Classify the preparation.
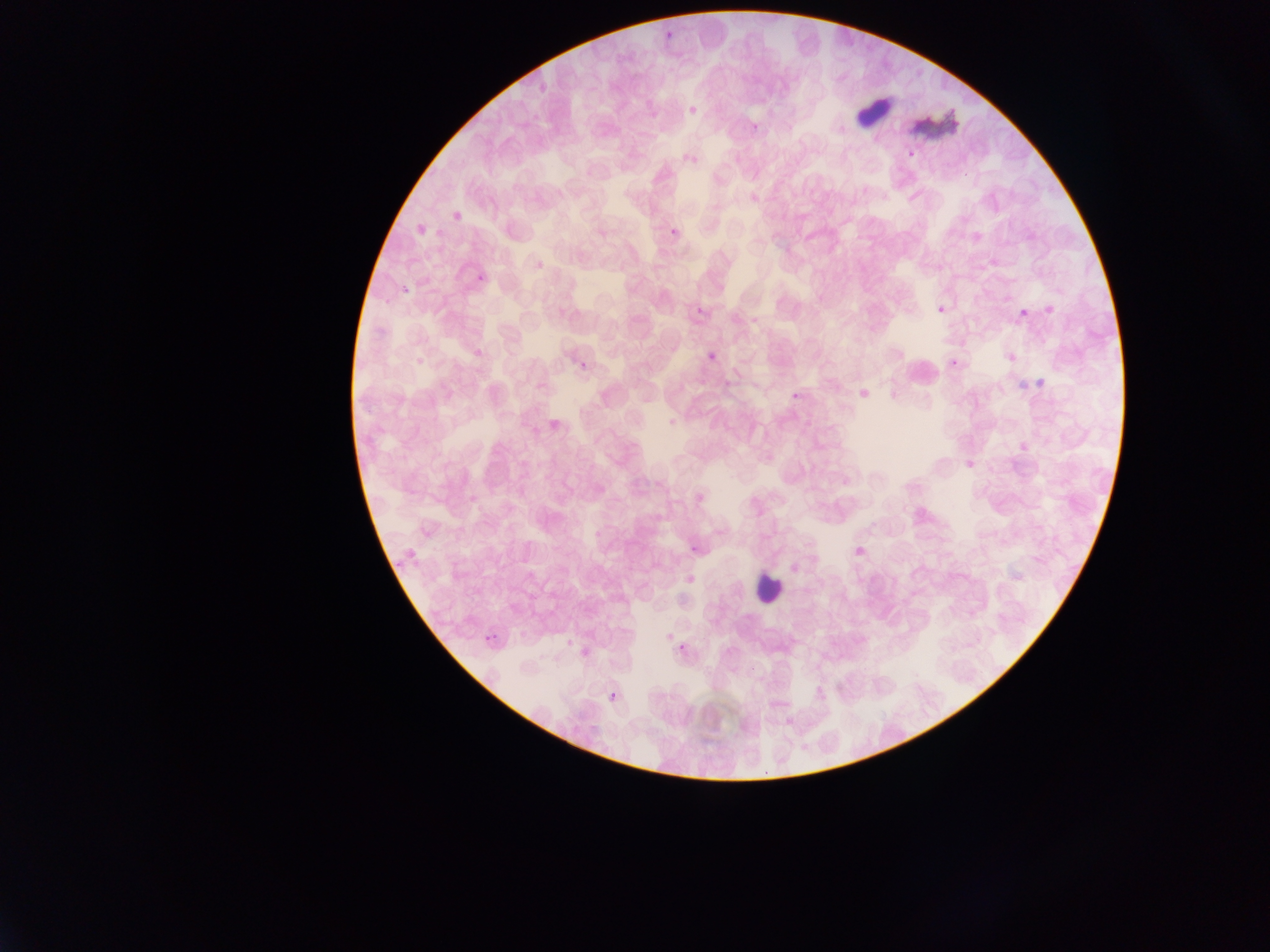
This is a thin smear.

Approximate bounding boxes as (left, top, right, bottom) in pixels. Malaria parasite locations: (664, 30, 679, 44), (536, 75, 550, 90), (688, 107, 697, 116), (751, 119, 764, 133), (907, 149, 916, 159), (450, 207, 467, 220), (415, 222, 428, 239), (667, 223, 683, 236), (475, 272, 489, 286), (400, 283, 412, 293), (1044, 300, 1058, 316), (937, 305, 945, 314), (696, 307, 705, 315), (1020, 307, 1028, 316), (471, 346, 488, 359), (1009, 351, 1021, 363), (708, 352, 716, 361), (950, 356, 961, 366), (580, 361, 588, 370), (722, 371, 732, 387), (1035, 375, 1049, 389), (1015, 378, 1027, 392), (791, 385, 802, 399), (857, 385, 875, 401), (546, 417, 563, 434), (667, 418, 677, 427), (962, 452, 977, 467), (468, 486, 480, 506), (689, 541, 699, 553), (856, 542, 867, 559), (393, 558, 407, 571), (483, 628, 500, 646), (677, 638, 688, 655), (607, 688, 618, 706). Artifact (stain precipitate or debris) locations: (911, 114, 958, 138). Leukocyte locations: (856, 86, 897, 129), (752, 569, 785, 604). Collected in Ghana. Image is 1270×952 pixels. Photographed through a microscope with a mobile-phone camera. One field of view.